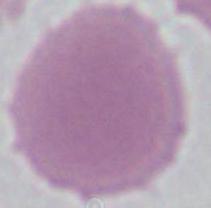

Captured at 1000x magnification. Photomicrograph. An erythrocyte is seen.